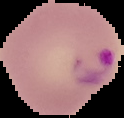

From a thin blood smear. Image is 124×118 pixels. Result: Plasmodium parasites detected. The area outside the segmented cell region is set to black.